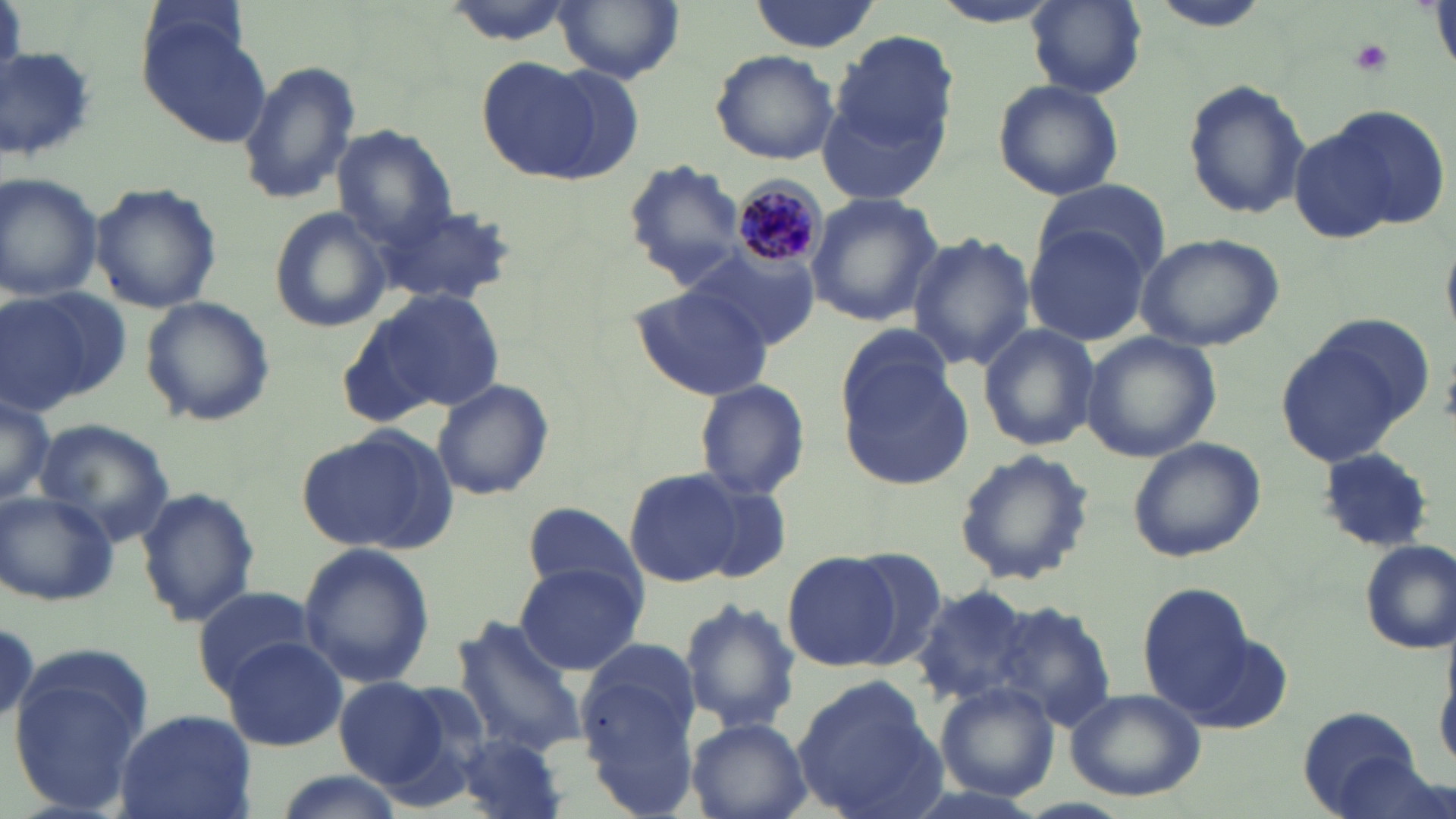
Approximate bounding boxes as (x1,y1)-(x2,y2) corner pairs in pixels. Plasmodium malariae-infected red blood cell locations: (732,174)-(832,278). Platelet locations: (1350,38)-(1393,75). Uninfected red blood cell locations: (555,0)-(684,83), (927,0)-(1068,29), (1027,0)-(1148,98), (1148,0)-(1277,32), (746,2)-(880,53), (140,13)-(273,150), (830,29)-(956,170), (0,45)-(97,161), (709,49)-(840,165), (233,57)-(363,207), (477,57)-(596,180), (536,66)-(646,183), (992,78)-(1126,202), (1180,78)-(1312,219), (817,89)-(952,205), (1295,106)-(1444,243), (334,127)-(455,244), (622,159)-(749,285), (0,173)-(103,303), (1031,178)-(1169,280), (90,185)-(223,314), (803,194)-(943,326), (381,201)-(519,309), (266,206)-(393,334), (1023,225)-(1153,347), (1135,230)-(1285,352), (909,231)-(1034,369), (688,247)-(819,351), (631,284)-(779,401), (365,285)-(507,414), (1,286)-(132,415), (138,296)-(277,428), (648,314)-(792,491), (1275,320)-(1430,471), (977,321)-(1101,453), (839,325)-(956,430), (1081,331)-(1221,464), (837,358)-(974,491), (431,379)-(554,502), (693,379)-(811,501), (0,391)-(56,509), (36,421)-(172,542), (295,424)-(457,556), (1125,435)-(1267,562), (952,451)-(1097,586), (624,467)-(743,587), (686,476)-(795,586), (135,485)-(260,627), (0,489)-(119,607), (521,501)-(646,602), (1356,540)-(1454,656), (297,542)-(436,689), (783,553)-(901,671), (514,561)-(646,675), (910,584)-(1035,704), (1138,584)-(1255,706), (192,587)-(321,694), (678,597)-(799,731), (990,599)-(1116,729), (450,619)-(589,762), (219,638)-(346,750), (579,640)-(698,787), (8,645)-(152,815), (793,673)-(948,819), (333,678)-(451,789), (934,682)-(1060,801), (1063,686)-(1207,803), (1297,706)-(1429,817), (114,709)-(257,819), (686,718)-(810,818), (447,731)-(571,819), (272,771)-(407,819). Slide-level diagnosis: Plasmodium malariae. One field of a larger specimen. Thin blood film. Optical microscopy. May-Grünwald-Giemsa-stained preparation. Image is 1456×819 pixels. 1000x magnification.